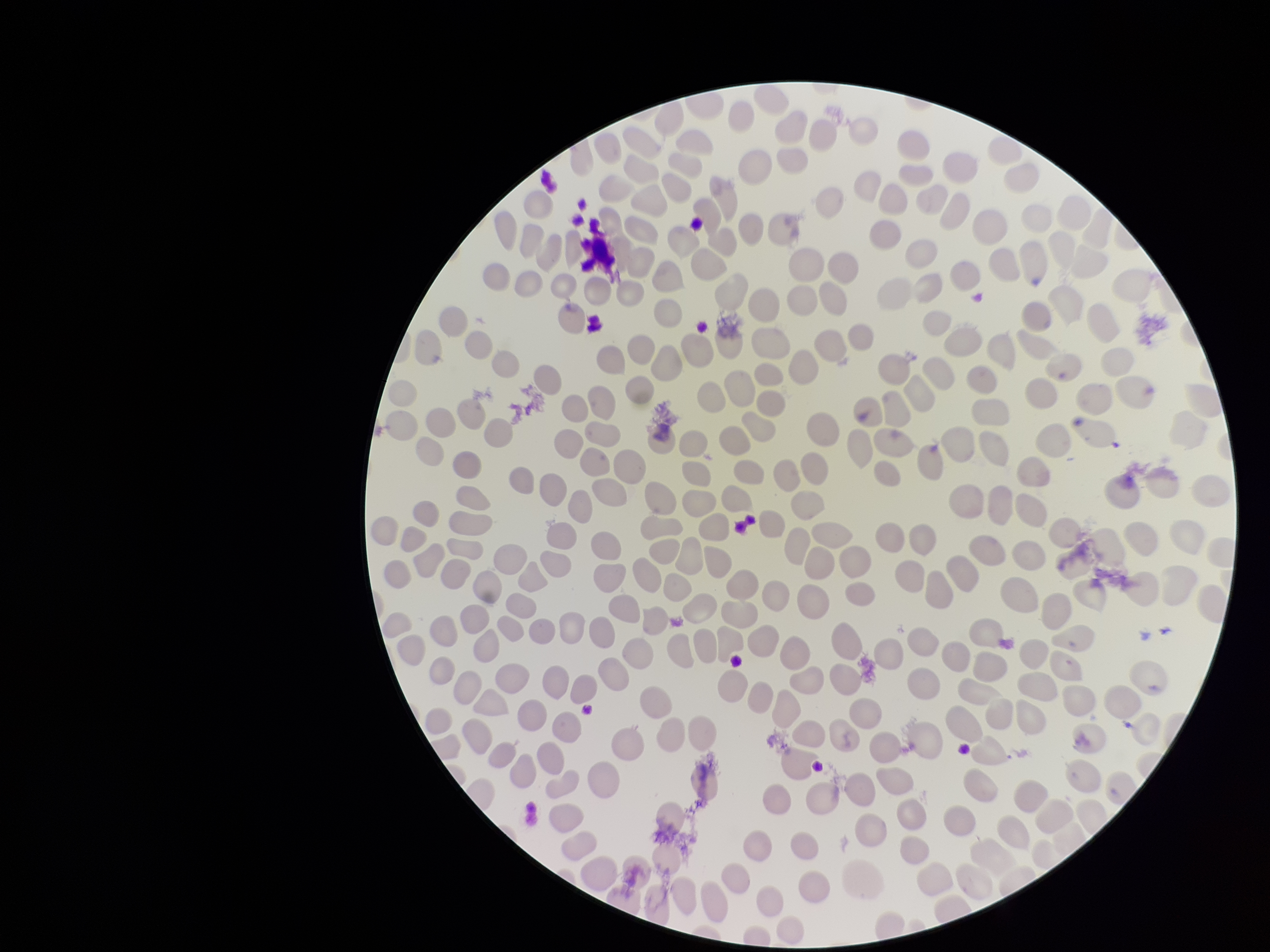
Image is 1270×952 pixels. Red blood cell count: 245. Patient malaria status: negative. One field from this slide. Preparation: thin. Giemsa stain. Parasitized red blood cell count: 0. Parasitized red blood cells: none seen. Smartphone photograph taken through the eyepiece of a microscope.